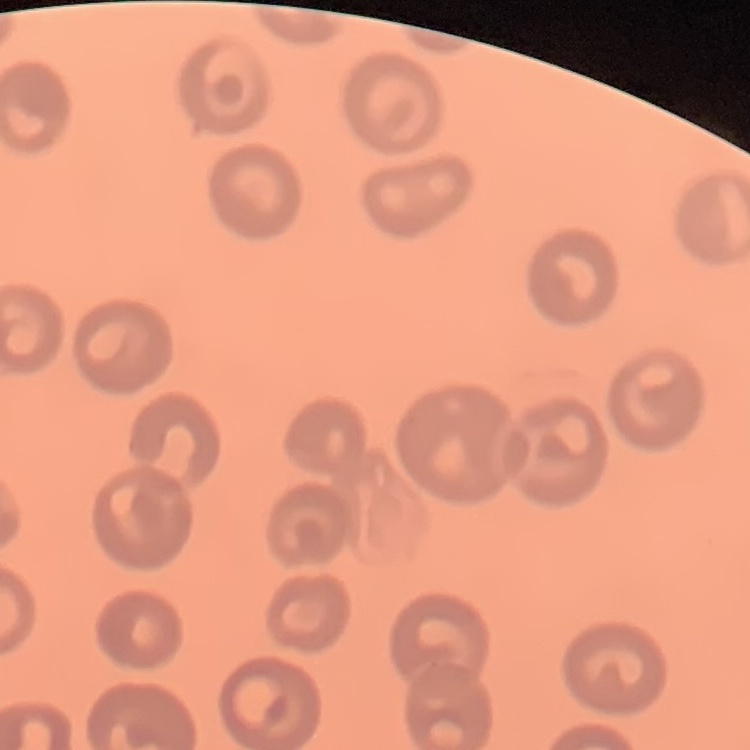

Summary:
  - Erythrocyte morphology: no rouleaux formation
  - Image type: one tile cut from a larger photomicrograph
  - Preparation: thin peripheral smear
  - Stain: Field's or Giemsa